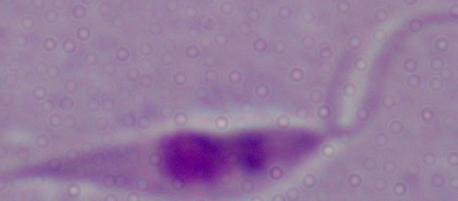
A Leishmania parasite is seen. Micrograph. Captured at 1000x magnification.